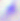
Toxoplasma gondii is seen. Photomicrograph. Captured at 400x magnification.